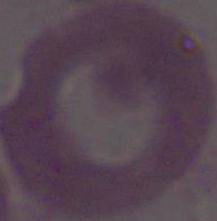

Summary:
  - Magnification: 1000x
  - Modality: micrograph
  - Identification: red blood cell